Assess the morphology of the red blood cells.
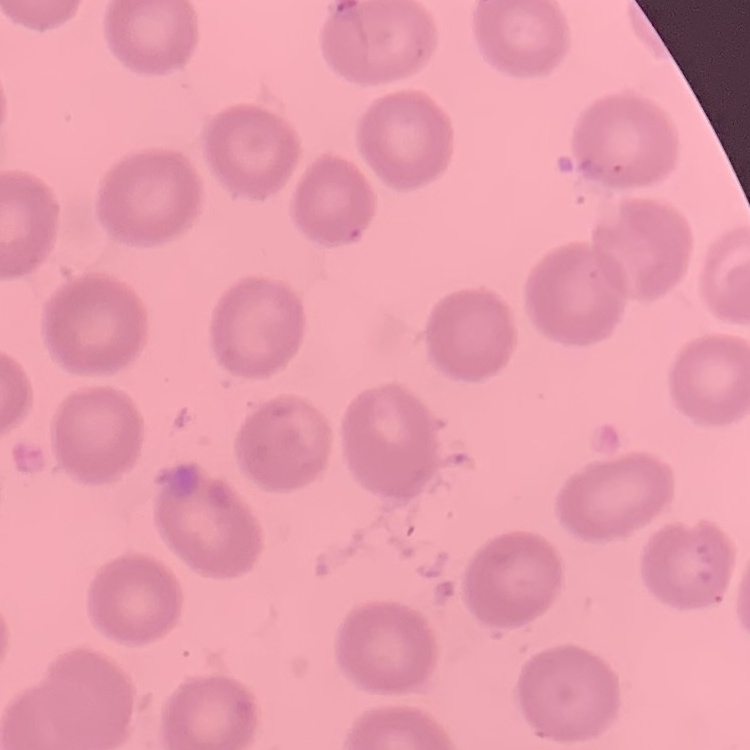
They show no rouleaux formation.

Thin blood smear. Stained with either Field's or Giemsa. Square crop of a larger photomicrograph.